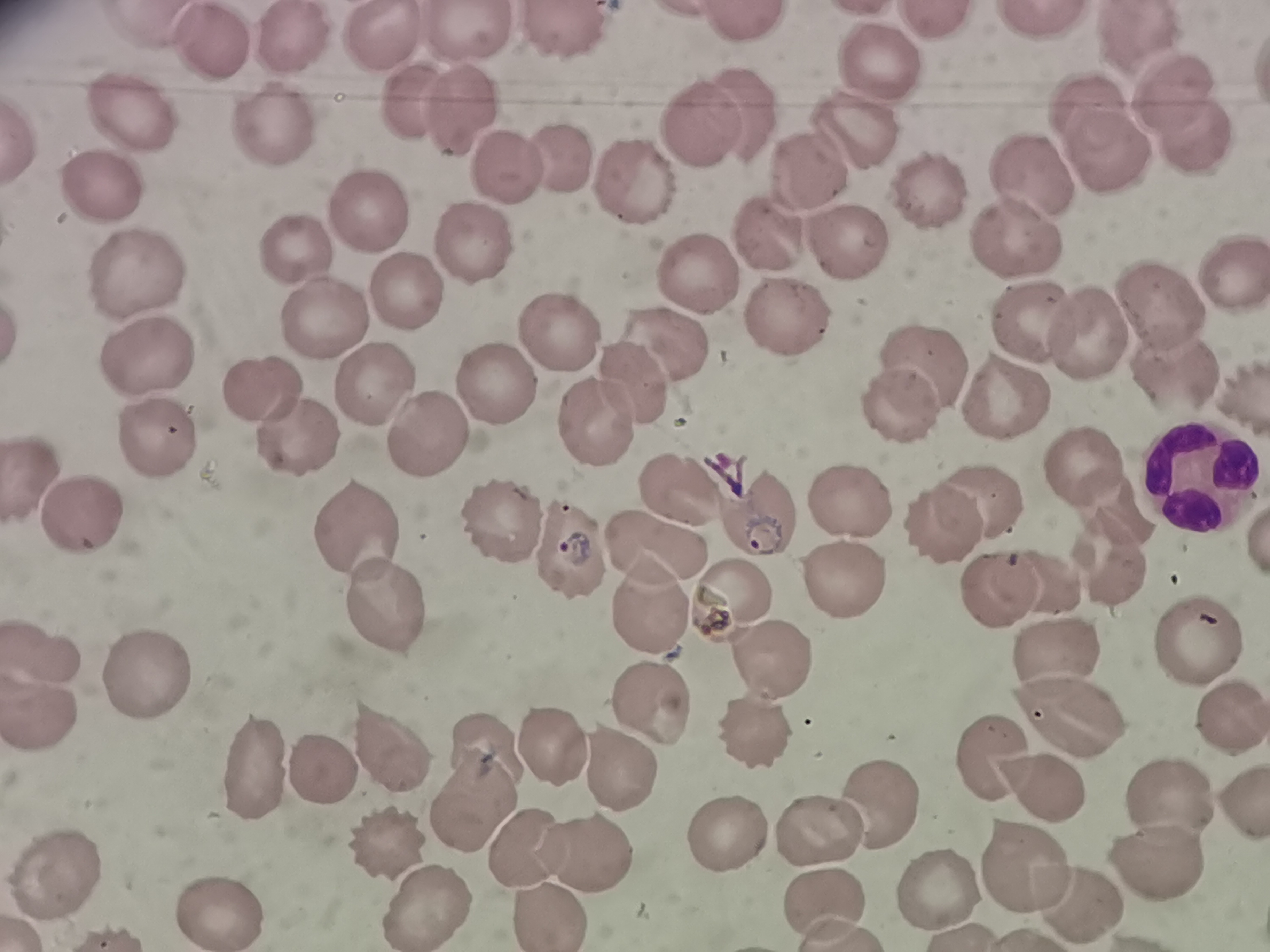 Approximate centers as [x, y] in pixels. Cell locations: [744, 21], [1033, 22], [568, 34], [466, 35], [382, 37], [1142, 37], [206, 39], [282, 43], [880, 66], [1169, 91], [417, 102], [462, 108], [1083, 108], [743, 115], [135, 116], [688, 117], [1185, 126], [268, 129], [855, 129], [1109, 151], [555, 152], [507, 164], [630, 172], [808, 172], [1041, 183], [93, 191], [926, 192], [366, 209], [1011, 236], [845, 237], [471, 238], [763, 238], [303, 253], [1230, 270], [134, 277], [689, 277], [409, 293], [1150, 300], [782, 314], [322, 319], [1037, 323], [553, 327], [1089, 333], [666, 341], [143, 358], [929, 362], [1170, 376], [630, 380], [377, 381], [501, 381], [262, 384], [1003, 395], [1238, 397], [898, 404], [585, 418], [421, 428], [156, 443], [300, 444], [1080, 460], [29, 466], [1188, 479], [686, 486], [846, 494], [984, 496], [1116, 511], [79, 515], [503, 522], [768, 523], [942, 525], [358, 530], [574, 544], [659, 546], [1102, 563], [840, 572], [996, 579], [1045, 581], [730, 598], [652, 599], [386, 601], [1195, 643], [1050, 648], [48, 650], [762, 660], [152, 685], [648, 699], [1221, 709], [40, 710], [1069, 712], [755, 729], [551, 734], [388, 746], [990, 748], [489, 754], [326, 765], [256, 766], [615, 766], [1046, 787], [1168, 797], [870, 798], [460, 806], [815, 824], [716, 827], [390, 839], [526, 843], [588, 845], [1019, 861], [1158, 861], [50, 882], [931, 885], [1078, 895], [421, 899], [816, 901], [225, 910], [542, 910]. Giemsa-stained preparation. Image is 1270×952 pixels. One field from this slide. Thin blood smear. Acquired by smartphone through the microscope eyepiece.